Classify this cell by malaria status.
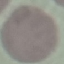

Uninfected.

Acquired by smartphone through the microscope eyepiece. Thin blood film. Giemsa stain. Cell patch, automatically extracted from a larger field of view and resized to 64 × 64 pixels.